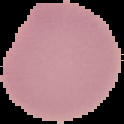
Summary:
  - Preparation: thin blood film
  - Result: negative for malaria parasites
  - Image type: segmented cell region with the area outside set to black
  - Image size: 124×124 pixels